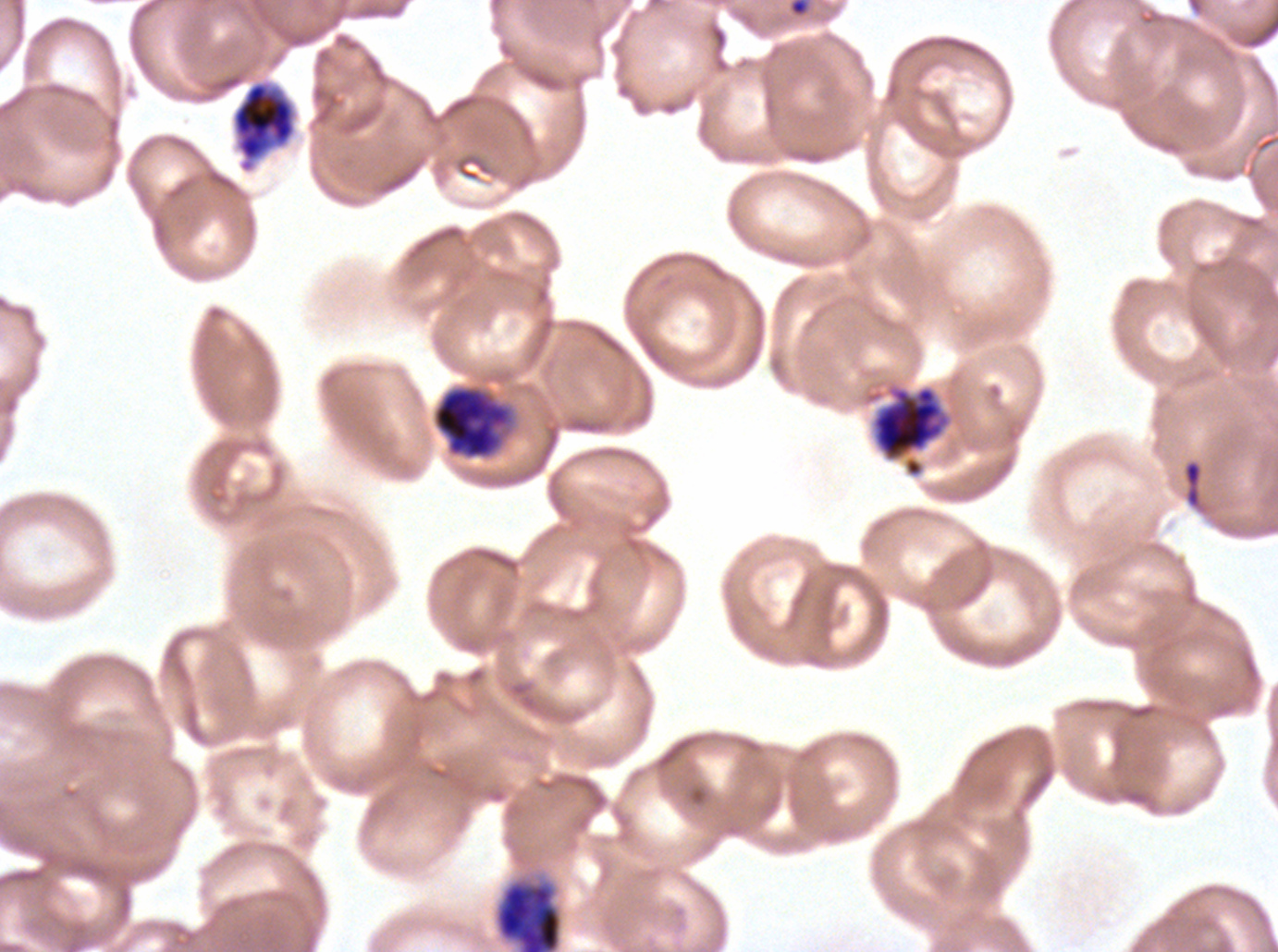
Approximate bounding rectangles given as corner coordinates in pixels from the top-left.
Summary:
  - Early schizont locations: (x1=433, y1=386, x2=510, y2=458), (x1=872, y1=386, x2=943, y2=459), (x1=497, y1=883, x2=561, y2=951)
  - Debris locations: (x1=787, y1=0, x2=812, y2=18), (x1=1182, y1=458, x2=1204, y2=511)
  - Late schizont locations: (x1=232, y1=81, x2=296, y2=172)
  - Stain: Giemsa
  - Preparation: thin blood film
  - Image size: 1278×952 pixels
  - Life-cycle stages observed: early schizont, late schizont
  - Specimen: P. falciparum cultured ex vivo for 24 to 48 hours, from a patient in The Gambia
  - Field of view: sub-image separated from a larger composite